State which parasite is depicted.
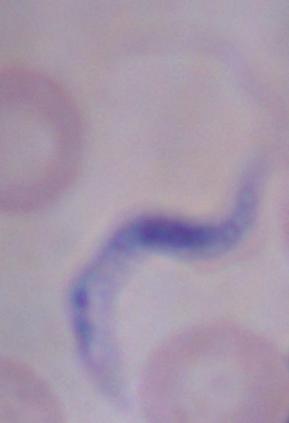
A trypanosome.

Micrograph. Captured at 1000x magnification.